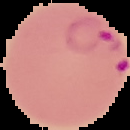 Malaria status: parasitized. Image is 130×130 pixels. From a thin blood film. The area outside the segmented cell region is set to black.